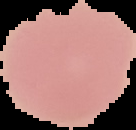
image size = 136×130 pixels
image type = cell region segmented out of the field of view; surrounding area masked to black
result = no malaria parasites detected
preparation = thin blood film